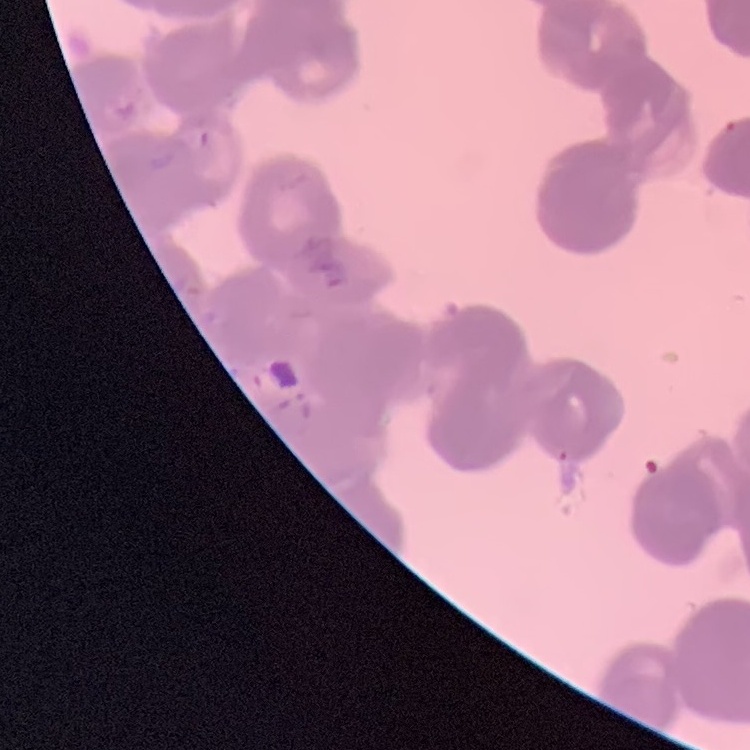
The red blood cells show rouleaux formation. Square crop of a larger photomicrograph. Field's or Giemsa stain. Thin blood smear.